Point out each Plasmodium parasite.
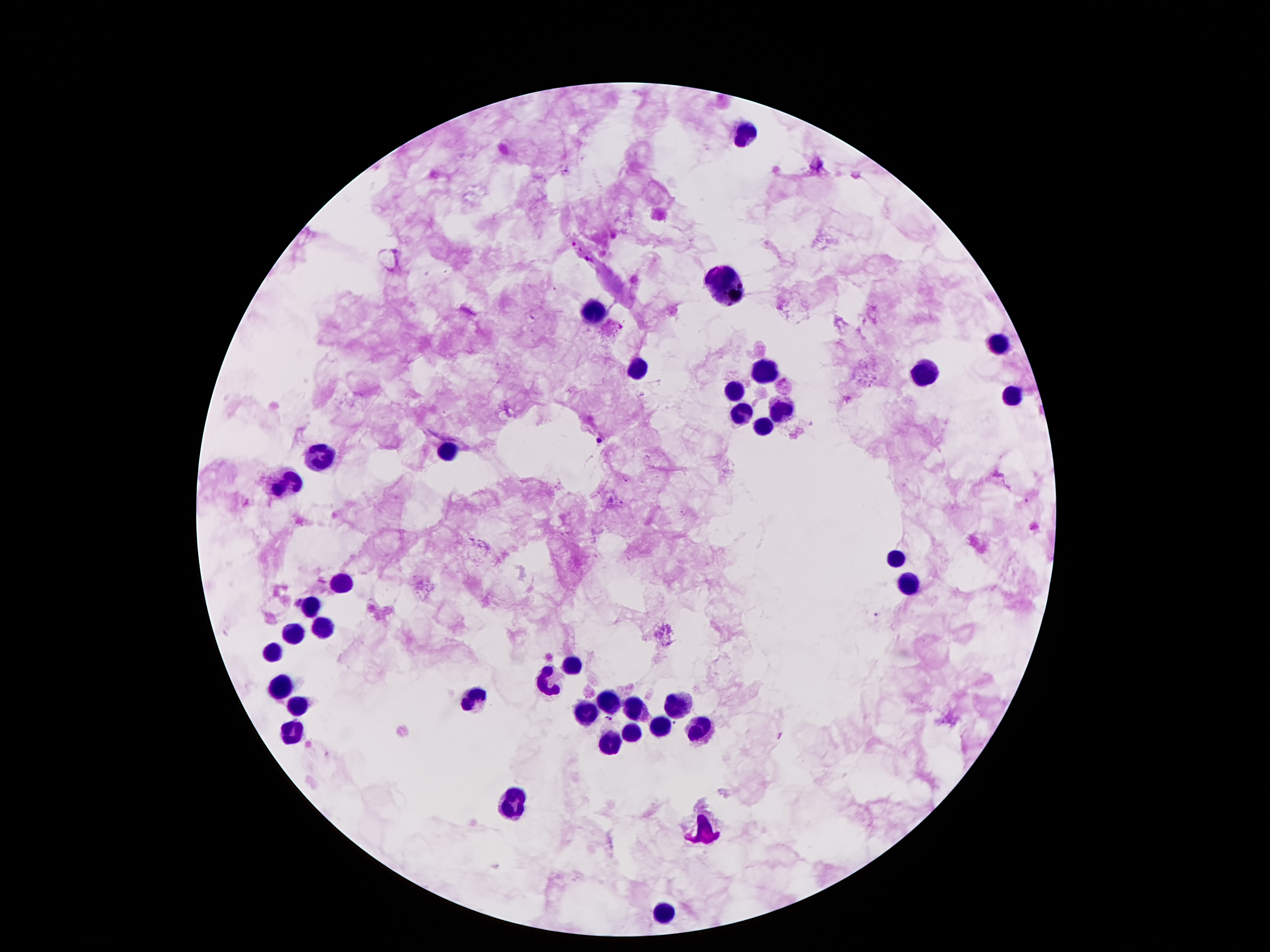

Approximate centers as [x, y] in pixels.
Plasmodium parasites: [573, 244], [586, 259], [598, 439], [296, 600], [609, 719], [675, 723].

{
  "magnification": "100x",
  "preparation": "thick blood film",
  "stain": "Giemsa",
  "image_size": "1270×952 pixels",
  "capture": "smartphone through the microscope eyepiece",
  "field_of_view": "single",
  "patient_malaria_status": "positive for Plasmodium falciparum",
  "leukocyte_locations": "approximate centers as [x, y] in pixels: [752, 133], [722, 282], [596, 312], [995, 346], [641, 369], [767, 373], [926, 373], [733, 390], [1014, 396], [779, 411], [739, 415], [764, 430], [449, 450], [321, 455], [288, 484], [895, 557], [344, 583], [907, 583], [311, 606], [323, 627], [292, 633], [273, 652], [569, 663], [548, 684], [281, 686], [470, 698], [607, 700], [676, 702], [300, 705], [584, 708], [634, 710], [659, 727], [699, 728], [632, 734], [288, 736], [611, 740], [515, 801], [708, 826], [664, 910]"
}